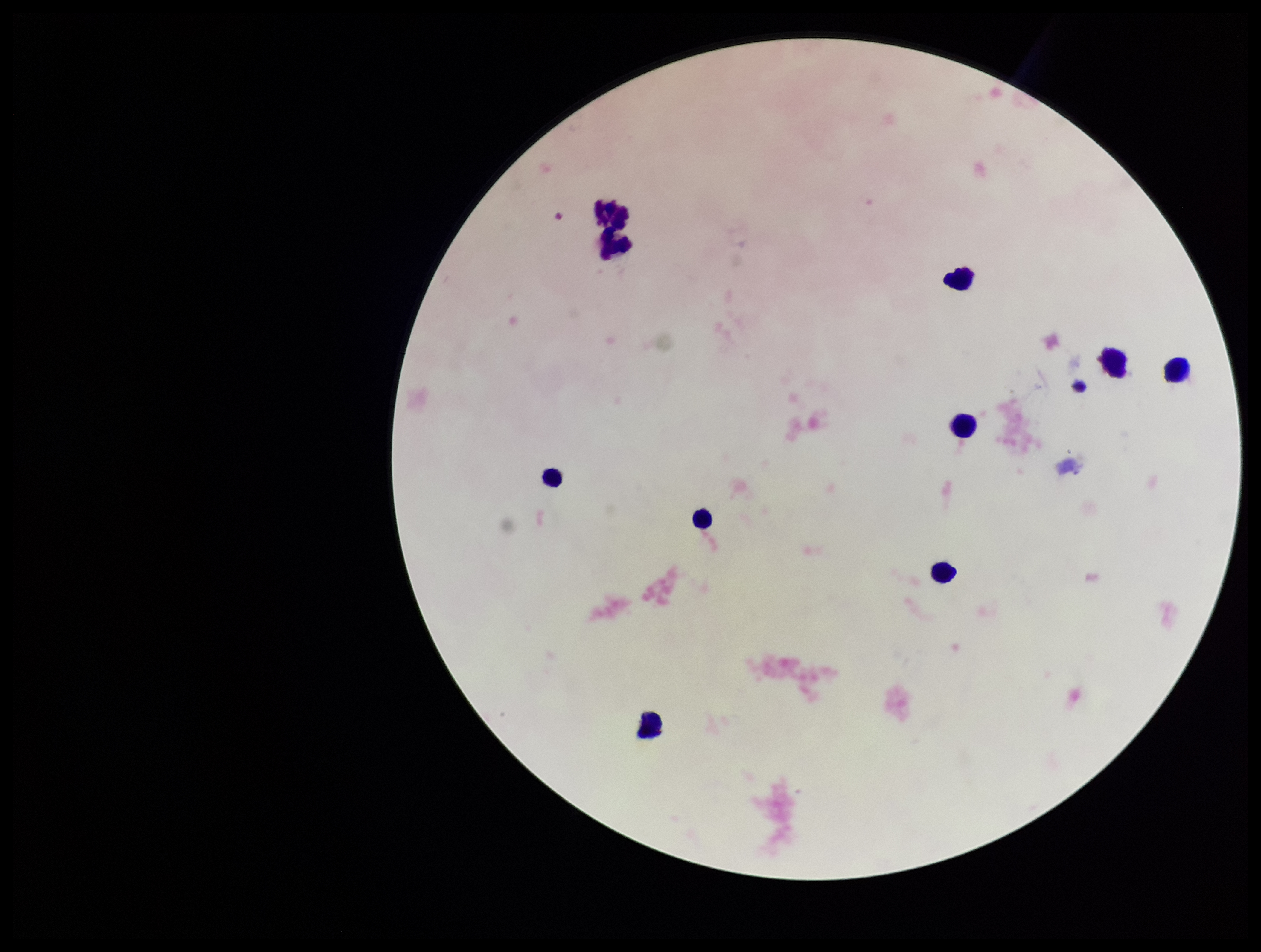

patient malaria status = negative
leukocyte count = 10
capture = smartphone photograph through the microscope eyepiece
preparation = thick smear
stain = Giemsa
image size = 1261×952 pixels
field of view = single
parasite count = 0
Plasmodium parasites = none seen